Outline every parasitised red blood cell.
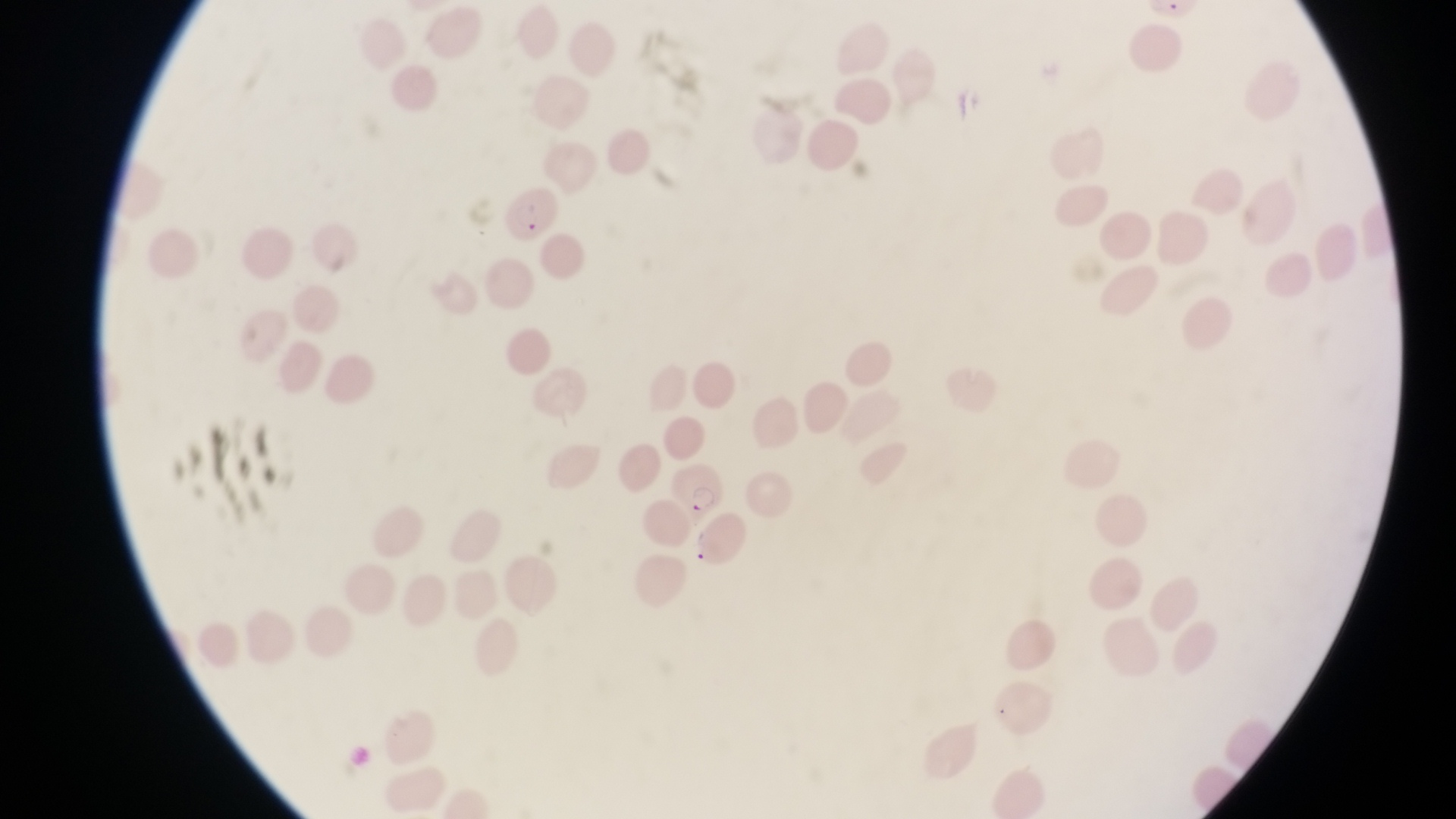

Approximate bounding boxes as left top right bottom in pixels.
Parasitised red blood cells: 502 188 560 244; 670 462 728 522.

Thin blood film. One field of view. Captured by a smartphone held over the eyepiece of an Olympus CX-23 microscope. Collected in Uganda. Image is 1456×819 pixels. At a magnification of 1000x.